Report the malaria status.
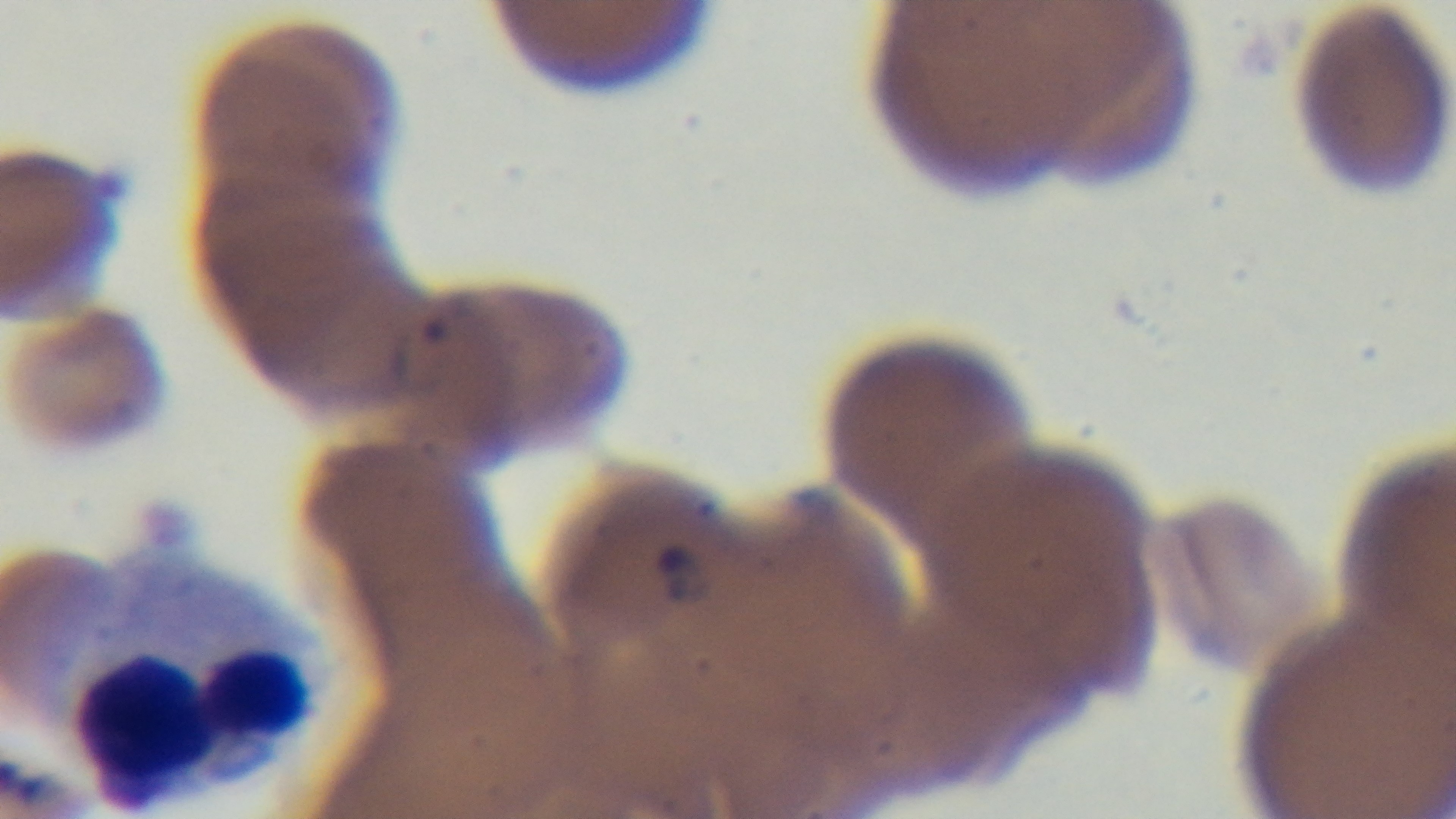

Infected.

preparation = thin blood film
modality = light microscopy
objective = 100x oil immersion
capture = mounted 4K digital camera
stain = Giemsa
field of view = single